Identify the cell.
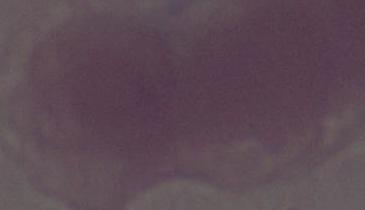
This is an erythrocyte.

modality = micrograph
magnification = 1000x